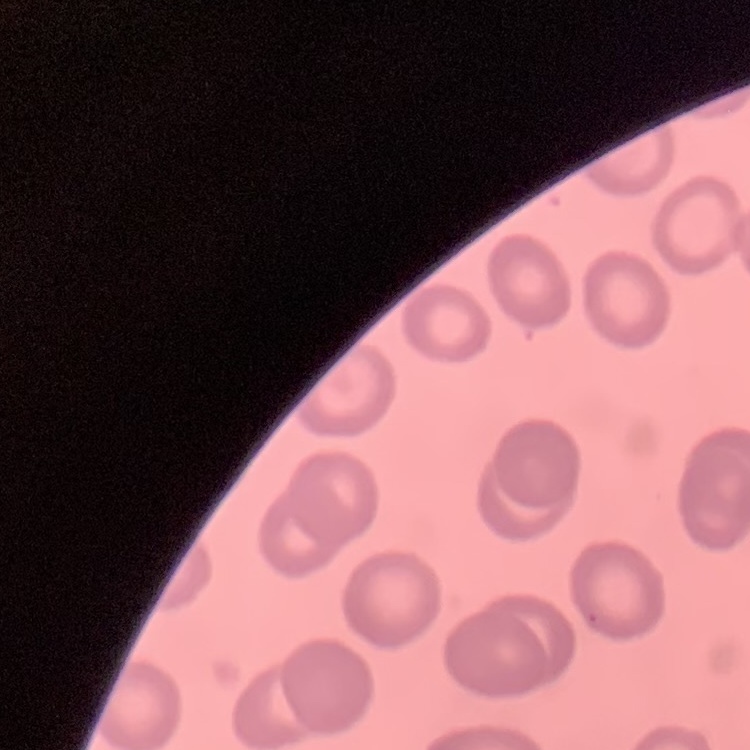

The erythrocytes show no rouleaux formation. Stained with either Field's or Giemsa. One tile cut from a larger photomicrograph. Thin peripheral smear.